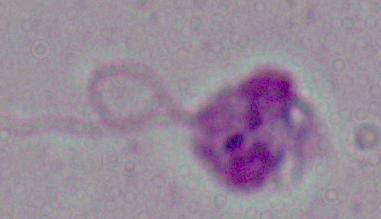

Photomicrograph. A Leishmania parasite is seen. Captured at 1000x magnification.